Locate every uninfected red blood cell.
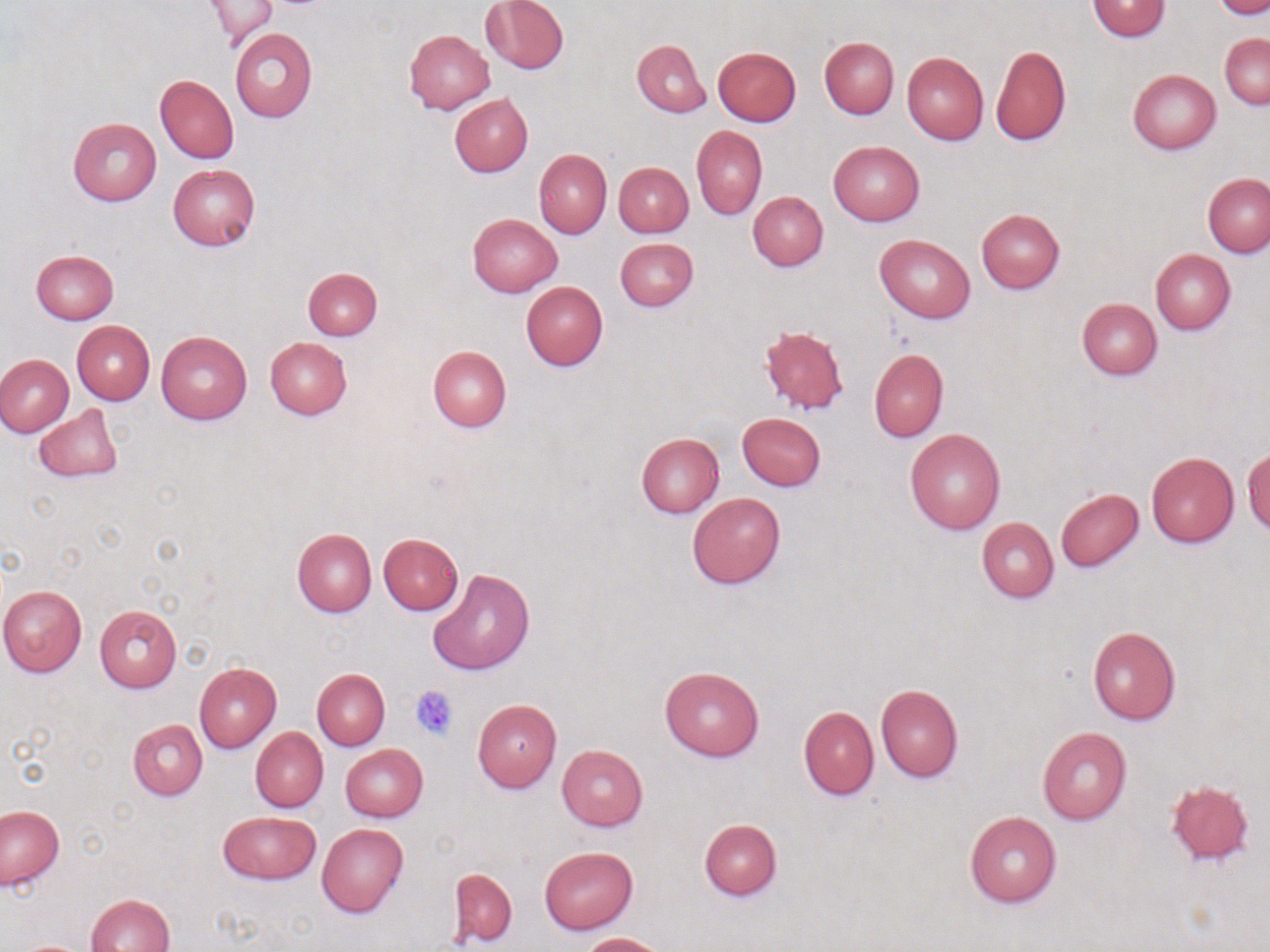
Approximate bounding boxes as (x1, y1, x2, y2) in pixels.
Uninfected red blood cells: (204, 0, 277, 46), (481, 0, 569, 74), (1087, 0, 1171, 41), (1213, 0, 1268, 20), (230, 27, 317, 123), (404, 28, 495, 115), (1220, 33, 1269, 110), (819, 36, 899, 119), (632, 38, 711, 118), (991, 45, 1071, 145), (712, 46, 802, 126), (901, 52, 989, 146), (1127, 69, 1220, 153), (156, 75, 238, 163), (449, 94, 532, 177), (67, 117, 161, 206), (691, 126, 767, 219), (828, 141, 925, 226), (534, 148, 611, 239), (614, 162, 694, 237), (168, 164, 260, 251), (1202, 173, 1270, 258), (748, 191, 828, 272), (976, 208, 1065, 293), (468, 213, 563, 296), (875, 234, 975, 322), (614, 238, 698, 311), (1150, 248, 1236, 334), (31, 249, 119, 324), (303, 267, 382, 340), (520, 281, 608, 371), (1076, 298, 1162, 380), (72, 321, 155, 405), (758, 323, 849, 415), (156, 331, 252, 424), (264, 337, 352, 419), (427, 345, 512, 432), (869, 349, 949, 442), (0, 354, 74, 436), (33, 403, 123, 483), (737, 412, 826, 491), (905, 428, 1005, 534), (636, 433, 724, 518), (1243, 447, 1270, 534), (1146, 453, 1239, 547), (1055, 488, 1144, 572), (688, 493, 785, 589), (976, 517, 1058, 603), (291, 528, 377, 616), (379, 533, 463, 616), (427, 569, 536, 676), (0, 586, 87, 676), (95, 605, 182, 693), (1087, 625, 1181, 726), (194, 663, 283, 754), (658, 664, 764, 761), (312, 669, 390, 750), (875, 683, 964, 782), (472, 698, 562, 792), (798, 706, 878, 800), (127, 718, 208, 800), (250, 726, 328, 812), (1036, 726, 1132, 825), (340, 744, 427, 822), (556, 745, 648, 831), (1166, 780, 1255, 867), (1, 805, 65, 891), (218, 811, 320, 884), (964, 811, 1062, 908), (699, 819, 782, 900), (317, 823, 408, 918), (539, 847, 638, 933), (447, 867, 517, 948), (86, 893, 176, 951), (579, 932, 670, 952).

Summary:
  - Platelet locations: (410, 685, 460, 741)
  - Slide-level diagnosis: no evidence of blood parasites
  - Image size: 1270×952 pixels
  - Magnification: 1000x
  - Modality: optical microscopy
  - Preparation: thin blood film
  - Field of view: one of a larger specimen
  - Stain: May-Grünwald-Giemsa